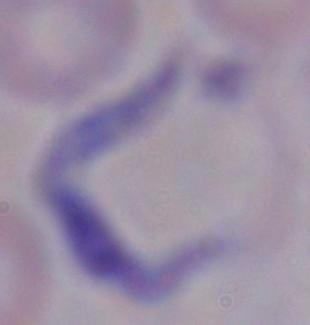 1000x magnification. Photomicrograph. A trypanosome is seen.